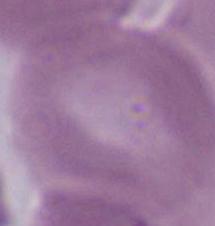

Summary:
  - Modality: photomicrograph
  - Identification: red blood cell
  - Magnification: 1000x